Name the parasite shown.
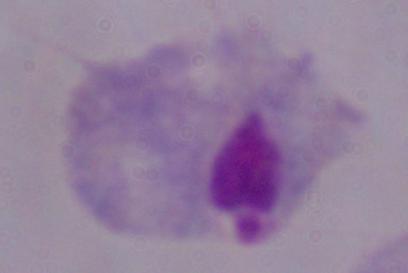
This is a trichomonad.

Micrograph. 1000x magnification.